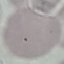
Result: negative for malaria parasites. Automatically extracted cell patch, resized to 64 × 64 pixels. Giemsa stain. Thin blood film. Acquired by smartphone through the microscope eyepiece.